Outline each Trypanosoma brucei.
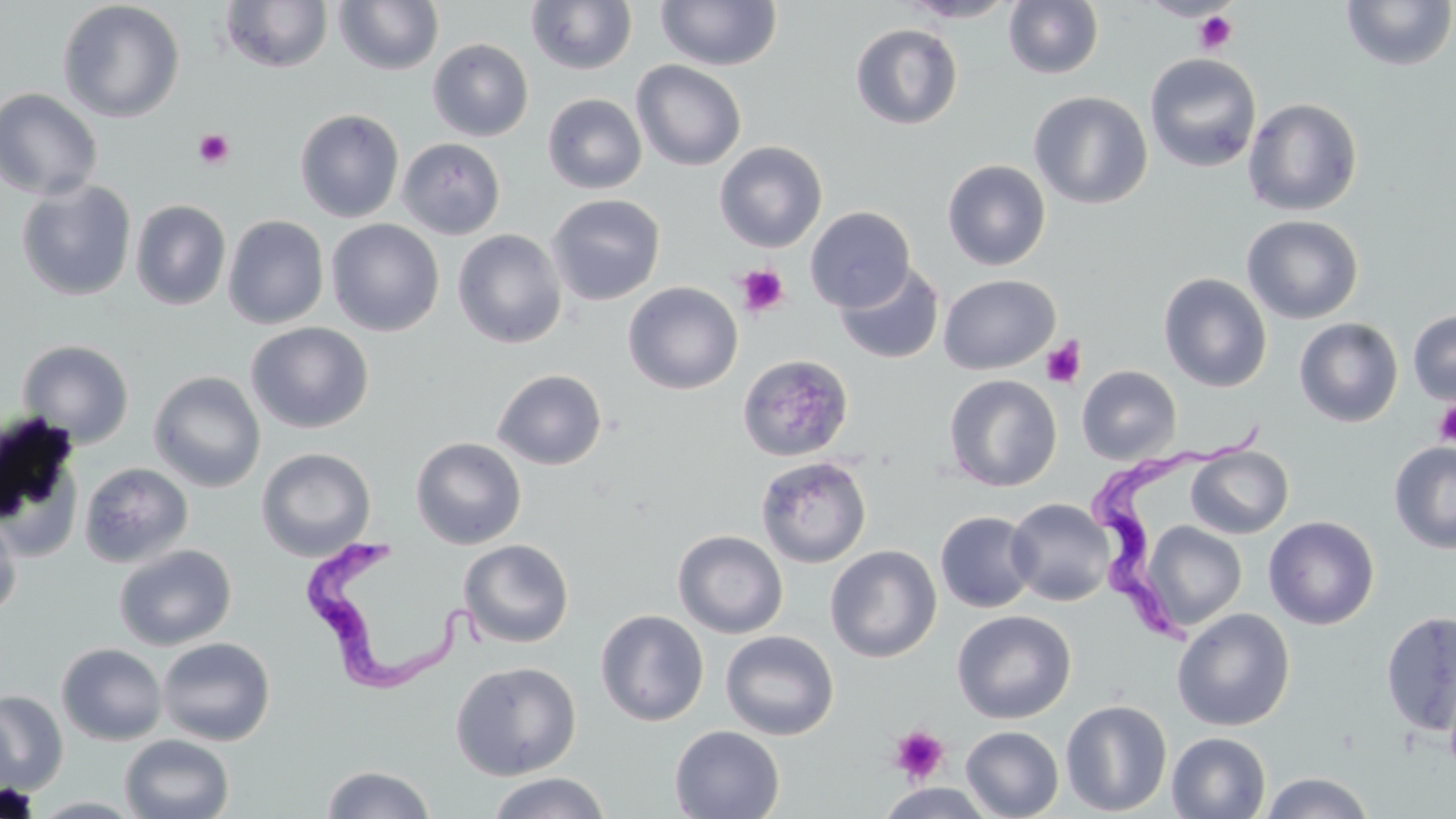
Approximate bounding boxes as named x1/y1/x2/y2 corners in pixels.
Trypanosoma brucei: (x1=1087, y1=418, x2=1272, y2=652), (x1=292, y1=531, x2=463, y2=698).

Platelet locations: (x1=1194, y1=10, x2=1238, y2=55), (x1=193, y1=129, x2=235, y2=169), (x1=736, y1=265, x2=789, y2=317), (x1=1040, y1=337, x2=1086, y2=387), (x1=1433, y1=400, x2=1456, y2=448), (x1=888, y1=725, x2=949, y2=784). Uninfected red blood cell locations: (x1=656, y1=0, x2=782, y2=70), (x1=898, y1=0, x2=1021, y2=23), (x1=1003, y1=0, x2=1104, y2=79), (x1=57, y1=1, x2=186, y2=123), (x1=219, y1=1, x2=333, y2=73), (x1=333, y1=1, x2=444, y2=75), (x1=526, y1=1, x2=638, y2=74), (x1=1340, y1=1, x2=1455, y2=71), (x1=1008, y1=5, x2=1120, y2=150), (x1=850, y1=23, x2=963, y2=130), (x1=427, y1=38, x2=534, y2=142), (x1=1144, y1=52, x2=1262, y2=173), (x1=631, y1=60, x2=747, y2=171), (x1=0, y1=88, x2=104, y2=201), (x1=1029, y1=90, x2=1152, y2=210), (x1=542, y1=93, x2=648, y2=194), (x1=1242, y1=97, x2=1363, y2=216), (x1=295, y1=108, x2=404, y2=223), (x1=397, y1=137, x2=506, y2=240), (x1=714, y1=140, x2=828, y2=252), (x1=942, y1=159, x2=1051, y2=271), (x1=16, y1=178, x2=137, y2=301), (x1=546, y1=194, x2=666, y2=306), (x1=130, y1=199, x2=232, y2=310), (x1=804, y1=206, x2=916, y2=312), (x1=222, y1=214, x2=329, y2=329), (x1=1242, y1=214, x2=1365, y2=324), (x1=326, y1=218, x2=445, y2=336), (x1=452, y1=229, x2=567, y2=349), (x1=833, y1=262, x2=945, y2=365), (x1=1158, y1=272, x2=1273, y2=392), (x1=938, y1=274, x2=1060, y2=375), (x1=623, y1=281, x2=743, y2=394), (x1=1407, y1=309, x2=1456, y2=406), (x1=1294, y1=318, x2=1403, y2=427), (x1=246, y1=322, x2=373, y2=433), (x1=17, y1=339, x2=135, y2=448), (x1=737, y1=353, x2=854, y2=462), (x1=1077, y1=365, x2=1181, y2=464), (x1=492, y1=369, x2=608, y2=470), (x1=148, y1=371, x2=266, y2=493), (x1=944, y1=374, x2=1062, y2=492), (x1=0, y1=414, x2=85, y2=558), (x1=410, y1=437, x2=527, y2=549), (x1=1389, y1=441, x2=1456, y2=554), (x1=1186, y1=445, x2=1293, y2=539), (x1=256, y1=447, x2=377, y2=562), (x1=755, y1=455, x2=872, y2=568), (x1=79, y1=461, x2=193, y2=568), (x1=1006, y1=498, x2=1115, y2=605), (x1=935, y1=511, x2=1039, y2=613), (x1=0, y1=512, x2=23, y2=619), (x1=1264, y1=515, x2=1380, y2=630), (x1=1140, y1=522, x2=1247, y2=632), (x1=673, y1=530, x2=789, y2=639), (x1=458, y1=538, x2=574, y2=648), (x1=113, y1=543, x2=237, y2=651), (x1=825, y1=544, x2=942, y2=663), (x1=1172, y1=607, x2=1295, y2=731), (x1=952, y1=609, x2=1077, y2=724), (x1=595, y1=610, x2=709, y2=726), (x1=1380, y1=610, x2=1456, y2=736), (x1=720, y1=630, x2=839, y2=741), (x1=156, y1=636, x2=276, y2=746), (x1=56, y1=642, x2=167, y2=746), (x1=450, y1=660, x2=581, y2=780), (x1=0, y1=690, x2=68, y2=794), (x1=1059, y1=699, x2=1173, y2=816), (x1=669, y1=725, x2=785, y2=819), (x1=961, y1=726, x2=1064, y2=819), (x1=1167, y1=732, x2=1271, y2=818), (x1=120, y1=734, x2=235, y2=819), (x1=320, y1=765, x2=436, y2=819), (x1=1259, y1=771, x2=1375, y2=818), (x1=487, y1=772, x2=612, y2=819), (x1=877, y1=783, x2=995, y2=819), (x1=28, y1=796, x2=145, y2=818). Slide-level diagnosis: Trypanosoma brucei. May-Grünwald-Giemsa stain. Single field of view. Optical microscopy. 1000x magnification. Image is 1456×819 pixels. Thin blood film.